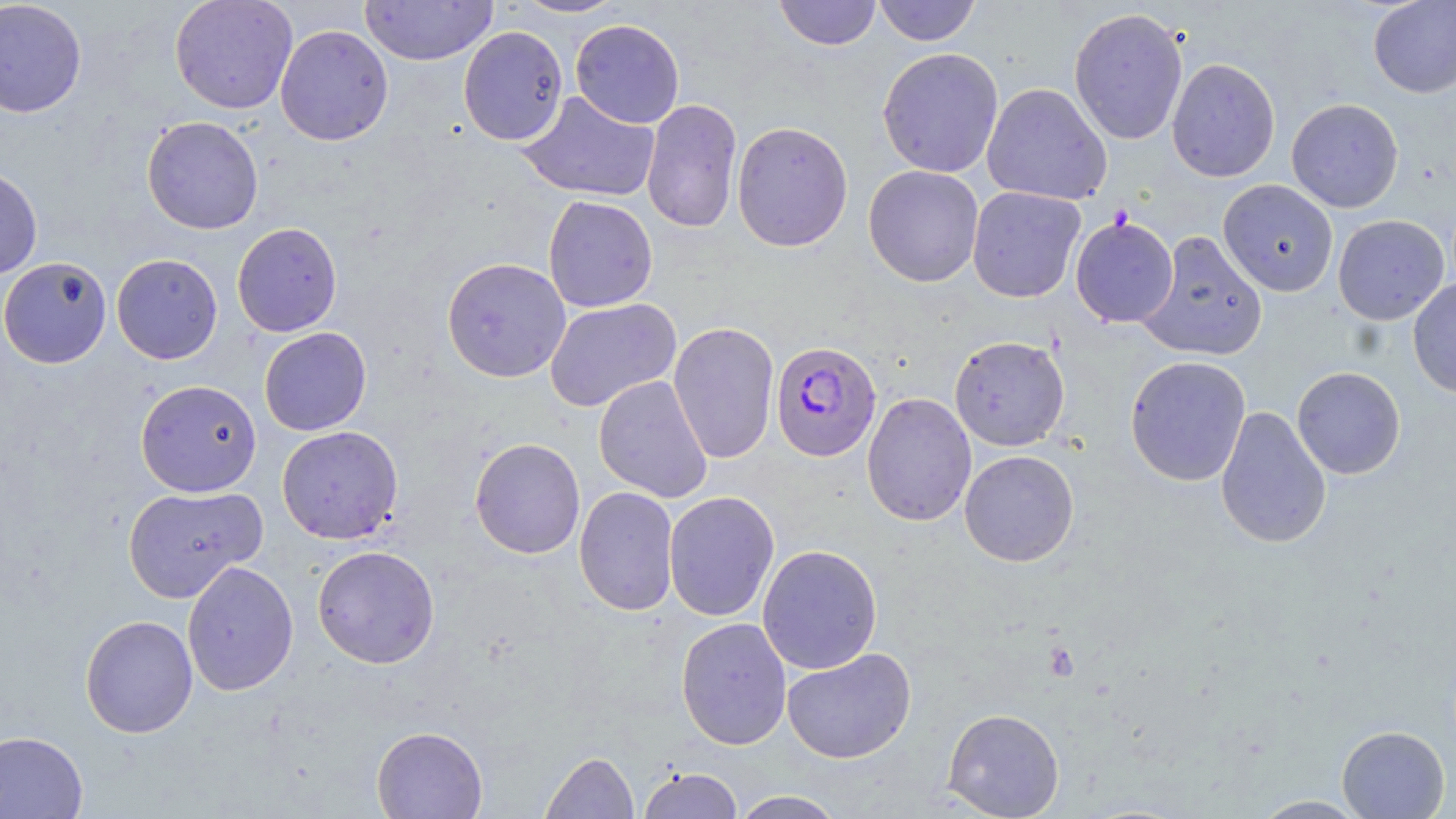
Plasmodium falciparum-infected red blood cell locations = approximate bounding boxes as (x1, y1, x2, y2) in pixels: (770, 341, 881, 462)
slide-level diagnosis = Plasmodium falciparum
modality = light microscopy
platelet locations = approximate bounding boxes as (x1, y1, x2, y2) in pixels: (1044, 640, 1080, 682)
preparation = thin blood film
magnification = 1000x
image size = 1456×819 pixels
uninfected red blood cell locations = approximate bounding boxes as (x1, y1, x2, y2) in pixels: (0, 0, 88, 118), (169, 0, 298, 114), (361, 0, 498, 66), (512, 0, 629, 18), (773, 0, 882, 51), (873, 0, 981, 46), (1368, 0, 1456, 98), (1068, 8, 1188, 145), (570, 19, 685, 128), (275, 24, 394, 145), (458, 25, 568, 146), (877, 47, 1004, 178), (1166, 57, 1280, 182), (981, 82, 1112, 205), (517, 90, 660, 202), (1286, 98, 1404, 213), (641, 99, 743, 233), (141, 115, 264, 235), (731, 120, 853, 252), (863, 165, 984, 287), (0, 166, 43, 279), (1218, 179, 1338, 296), (967, 186, 1086, 303), (542, 195, 658, 312), (1333, 214, 1449, 325), (1070, 215, 1179, 328), (232, 222, 343, 337), (1138, 231, 1268, 361), (111, 253, 223, 364), (0, 257, 112, 368), (442, 257, 571, 383), (1407, 278, 1456, 398), (544, 298, 681, 412), (668, 321, 779, 464), (259, 327, 371, 436), (949, 335, 1070, 451), (1125, 355, 1251, 487), (1292, 366, 1406, 479), (593, 375, 713, 503), (135, 379, 262, 497), (861, 392, 977, 527), (1214, 405, 1332, 550), (276, 425, 404, 544), (470, 437, 585, 559), (959, 449, 1079, 567), (122, 485, 267, 603), (573, 486, 679, 617), (663, 491, 780, 621), (757, 544, 883, 674), (312, 545, 440, 669), (182, 561, 299, 695), (80, 614, 198, 737), (676, 617, 792, 750), (781, 647, 917, 764), (942, 707, 1065, 819), (371, 725, 488, 818), (1336, 725, 1450, 818), (0, 730, 89, 818), (540, 751, 639, 818), (638, 767, 743, 818), (730, 790, 845, 818), (1252, 795, 1370, 818)
field of view = single
stain = May-Grünwald-Giemsa